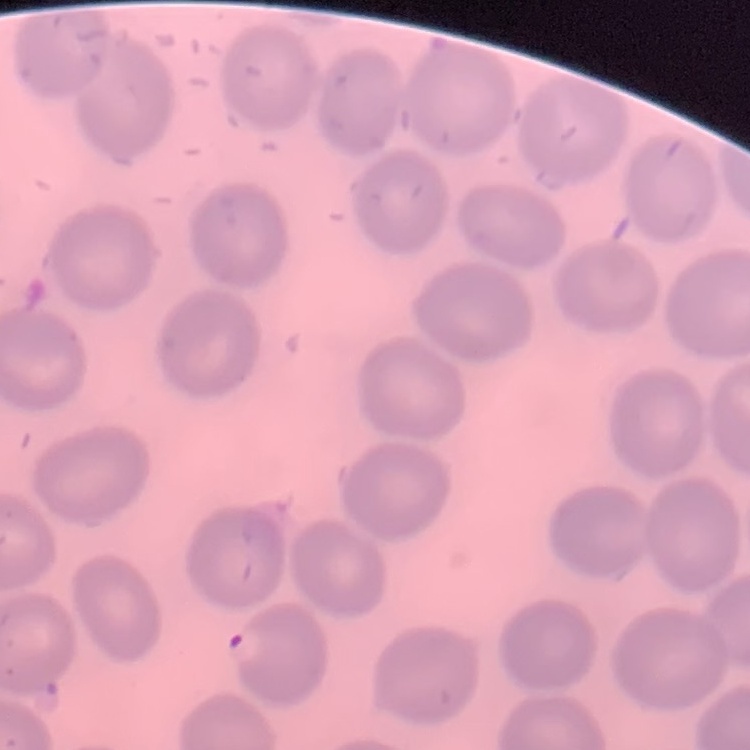
The erythrocytes exhibit no rouleaux formation. Field's or Giemsa stain. One tile cut from a larger photomicrograph. Thin peripheral smear.